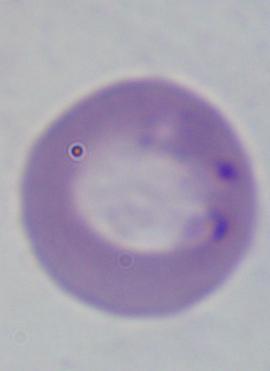

Photomicrograph. Captured at 1000x magnification. A Babesia parasite is seen.